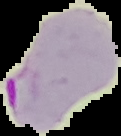

Summary:
  - Preparation: thin blood film
  - Malaria status: parasitized
  - Image size: 121×136 pixels
  - Image type: cell region segmented out of the field of view; surrounding area masked to black